Comment on the morphology of the red blood cells.
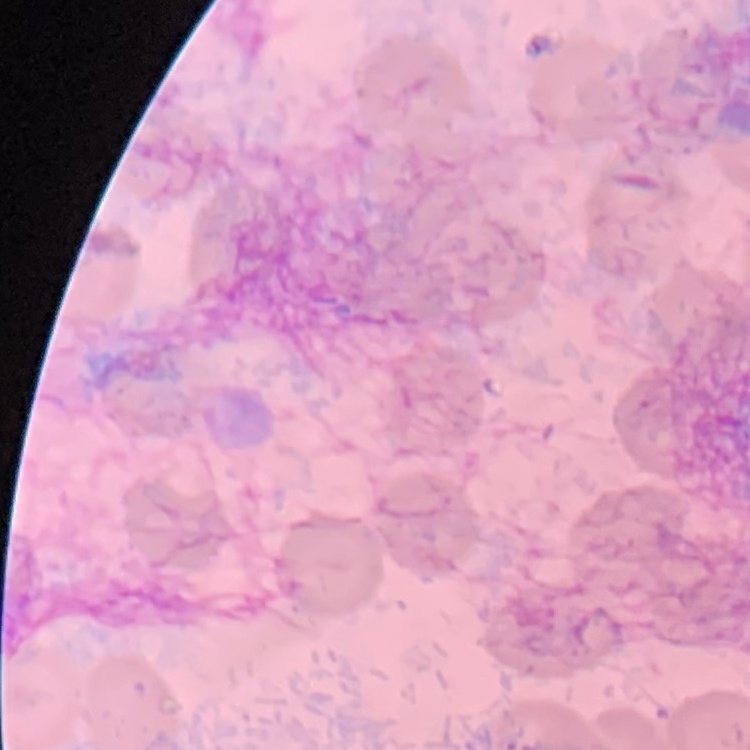

They show no rouleaux formation.

One tile cut from a larger photomicrograph. Field's or Giemsa stain. Thin blood film.